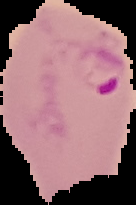

Summary:
  - Preparation: thin blood smear
  - Image type: cell region segmented out of the field of view; surrounding area masked to black
  - Image size: 136×205 pixels
  - Malaria status: parasitized